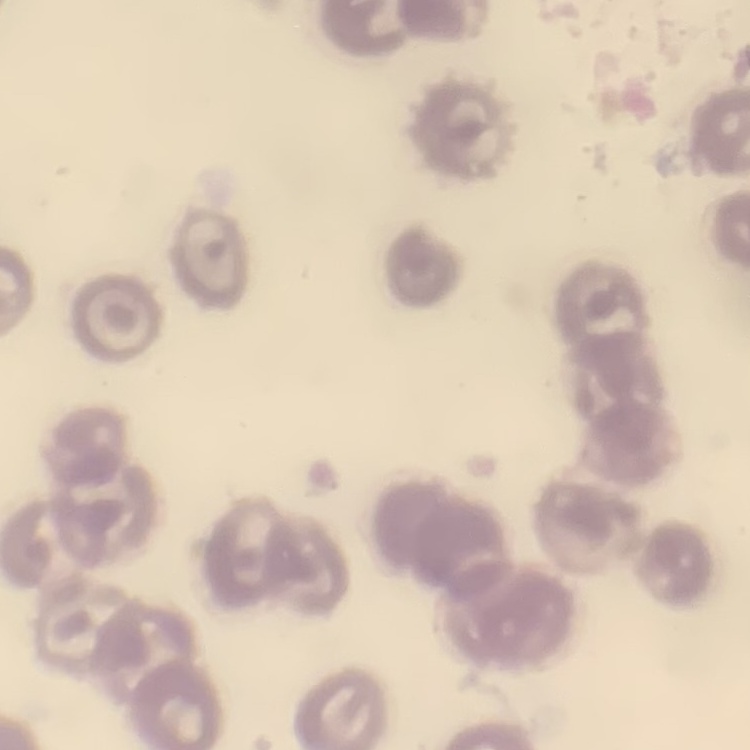

The erythrocytes show no rouleaux formation. One tile cut from a larger photomicrograph. Thin blood smear. Field's or Giemsa stain.